Assess this cell for malaria.
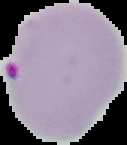

Parasitized.

Cell region segmented out of the field of view; the surrounding area is masked to black. Image is 127×145 pixels. From a thin blood film.